Give a bounding box for every malaria parasite, every leukocyte, and every artifact (stain precipitate or debris).
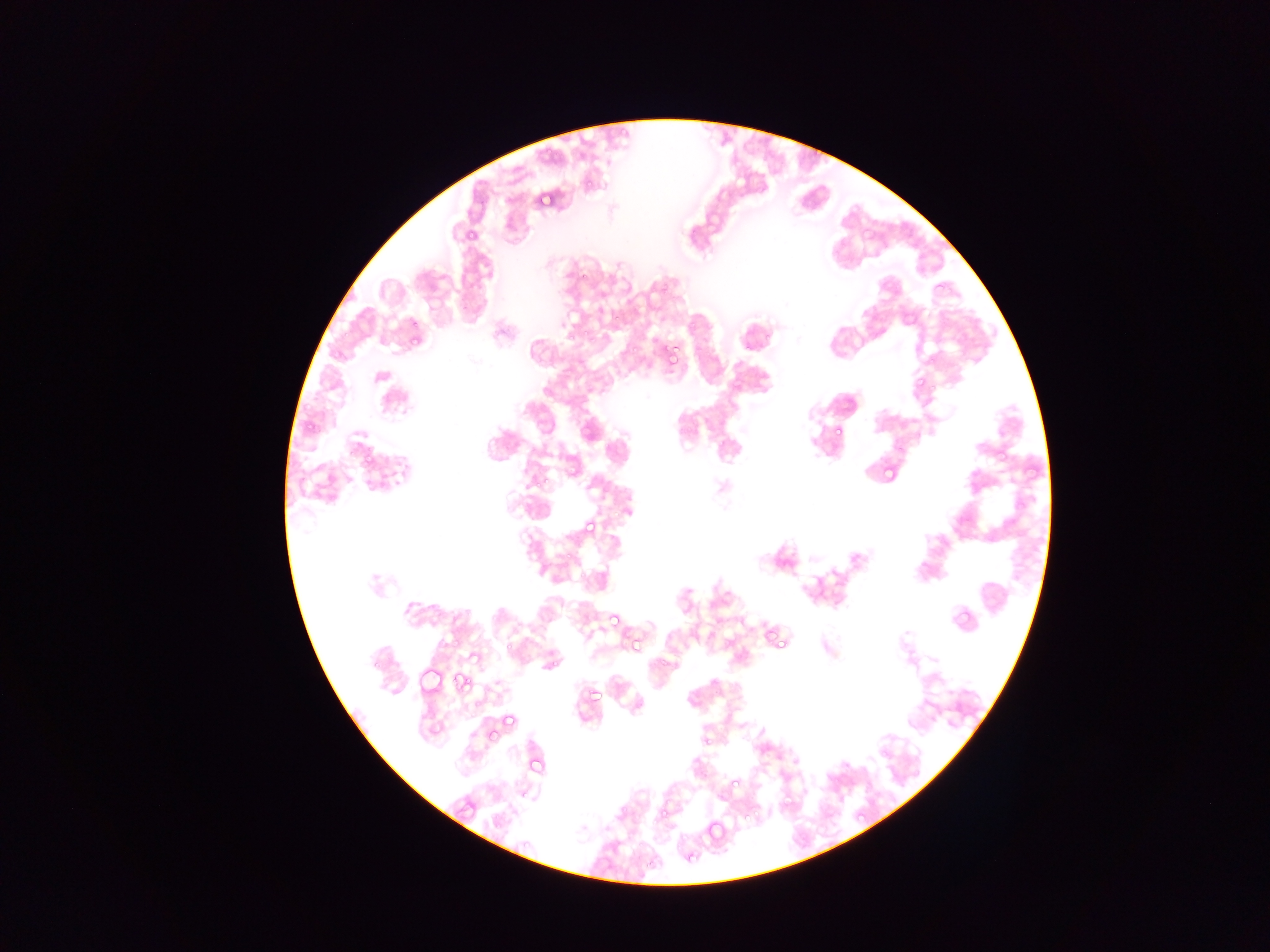

Approximate bounding boxes as [left, top, right, bottom] in pixels.
Malaria parasites: [811, 147, 822, 160], [582, 180, 597, 190], [537, 188, 555, 205], [460, 226, 475, 245], [579, 271, 589, 286], [610, 309, 620, 320], [904, 310, 917, 320], [408, 317, 419, 328], [583, 327, 592, 338], [336, 333, 346, 343], [565, 334, 575, 343], [405, 335, 421, 353], [661, 344, 677, 358], [927, 354, 937, 364], [913, 376, 926, 390], [301, 421, 314, 441], [832, 424, 843, 435], [346, 440, 361, 463], [997, 446, 1010, 456], [361, 456, 374, 469], [879, 463, 895, 479], [533, 475, 550, 490], [583, 519, 599, 536], [564, 548, 571, 558], [952, 607, 971, 625], [607, 612, 621, 627], [762, 625, 776, 640], [628, 634, 644, 657], [772, 635, 792, 652], [501, 639, 514, 654], [467, 651, 482, 665], [549, 660, 558, 670], [453, 673, 471, 691], [586, 685, 602, 701], [497, 712, 521, 735], [485, 726, 500, 740], [701, 735, 712, 746], [527, 755, 543, 772], [729, 781, 742, 793], [618, 806, 629, 818], [659, 809, 668, 822], [855, 811, 866, 822], [704, 817, 726, 842] | approximate [x, y] pixel centers of objects too small to bound: [745, 819].
No leukocytes observed.

country = Ghana
preparation = thin blood smear
image size = 1270×952 pixels
field of view = single
capture = mobile-phone photograph through a microscope